Assess the morphology of the erythrocytes.
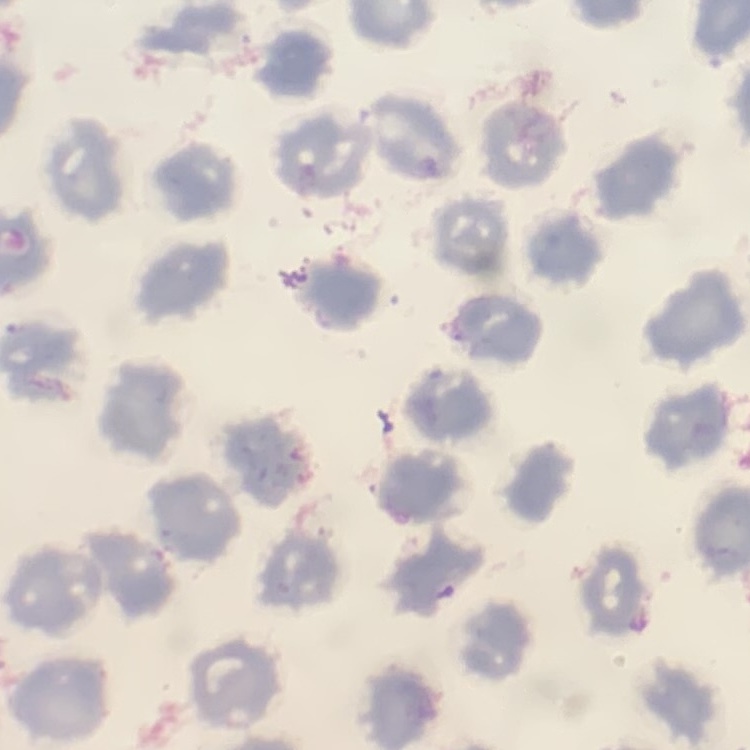
No rouleaux formation.

Summary:
  - Image type: square crop of a larger photomicrograph
  - Preparation: thin blood smear
  - Stain: Field's or Giemsa